Give the location of every parasitized RBC.
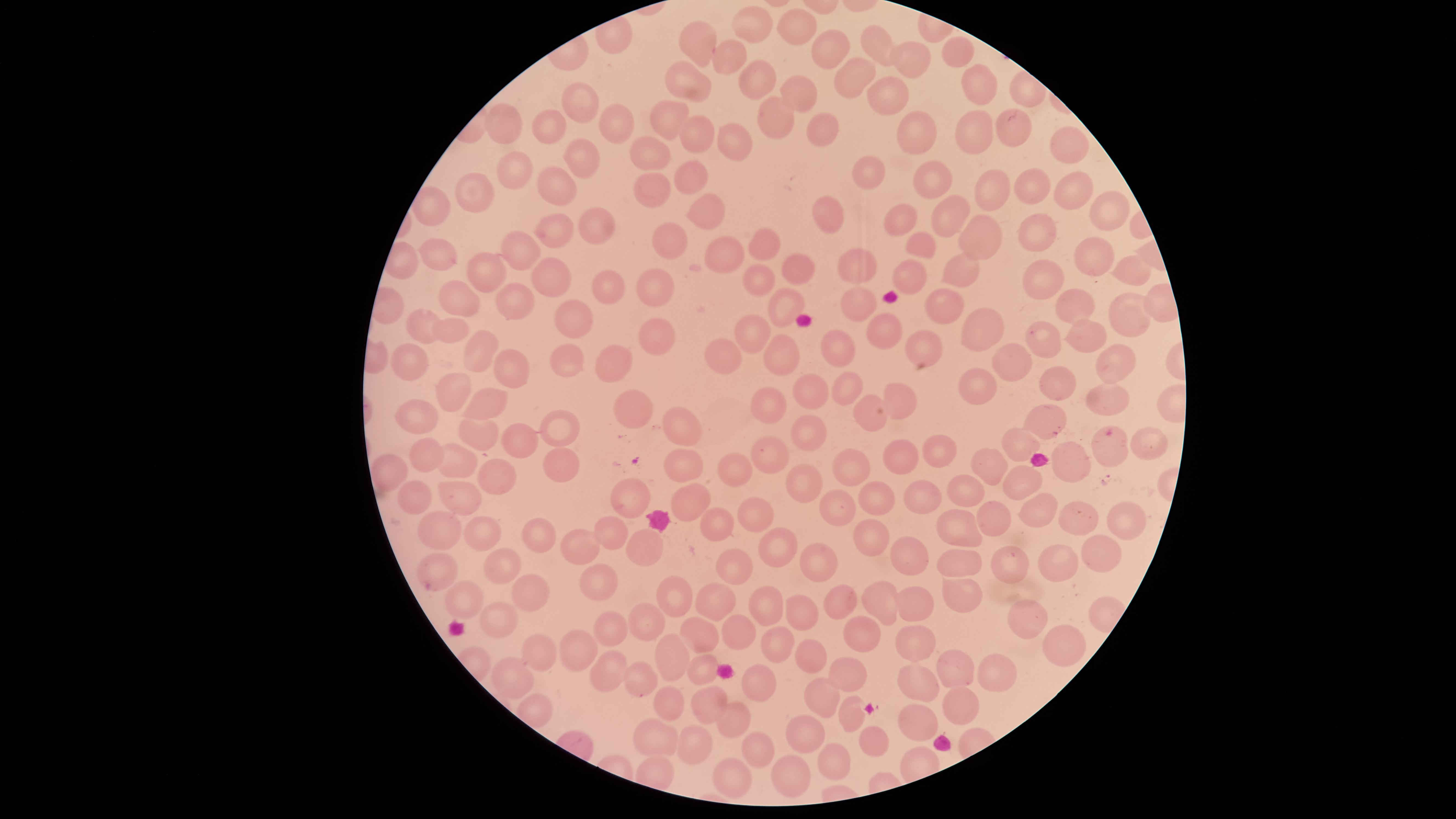
Approximate marker points as (x, y) in pixels.
Parasitized RBCs: (428, 586).

Approximate marker points as (x, y) in pixels. Uninfected RBCs: (754, 24), (801, 28), (699, 37), (875, 45), (831, 47), (960, 49), (729, 55), (913, 57), (851, 75), (755, 81), (688, 83), (976, 86), (799, 88), (883, 95), (578, 110), (666, 116), (774, 119), (615, 126), (817, 126), (1009, 127), (691, 129), (912, 129), (549, 131), (975, 132), (508, 133), (738, 136), (1066, 144), (656, 145), (579, 156), (519, 168), (688, 169), (872, 173), (931, 177), (557, 182), (654, 184), (1033, 187), (478, 190), (989, 190), (1063, 190), (707, 206), (1106, 206), (832, 209), (954, 216), (901, 221), (597, 225), (1039, 227), (557, 232), (980, 235), (667, 237), (923, 247), (730, 248), (765, 248), (441, 253), (518, 255), (1091, 257), (852, 264), (959, 267), (487, 268), (1130, 270), (798, 272), (760, 276), (910, 276), (553, 277), (1041, 277), (602, 284), (660, 285), (464, 296), (511, 302), (784, 304), (862, 304), (1072, 306), (944, 308), (1122, 309), (429, 320), (573, 320), (983, 324), (455, 328), (660, 333), (886, 334), (758, 335), (1048, 338), (1086, 338), (929, 342), (835, 343), (482, 344), (571, 354), (787, 354), (727, 359), (1116, 359), (1012, 361), (412, 362), (617, 364), (510, 370), (1056, 379), (979, 382), (847, 386), (459, 388), (813, 388), (898, 397), (1102, 399), (773, 403), (488, 404), (640, 406), (874, 409), (418, 414), (563, 417), (1046, 422), (685, 423), (806, 429), (481, 431), (525, 436), (1027, 441), (1148, 444), (428, 450), (939, 451), (1107, 452), (768, 457), (1073, 457), (906, 458), (982, 462), (455, 463), (558, 463), (857, 465), (736, 467), (494, 471), (683, 472), (391, 473), (1021, 479), (803, 482), (973, 487), (925, 492), (410, 495), (465, 495), (876, 497), (628, 498), (690, 503), (841, 506), (755, 510), (1037, 511), (1075, 517), (991, 520), (717, 524), (1116, 525), (957, 526), (440, 529), (477, 533), (538, 533), (612, 534), (873, 540), (581, 543), (644, 545), (778, 545), (1093, 546), (909, 550), (967, 556), (813, 562), (1052, 562), (724, 563), (1016, 563), (501, 567), (598, 581), (954, 595), (672, 596), (527, 597), (839, 597), (466, 599), (879, 599), (716, 600), (769, 601), (920, 608), (803, 610), (1030, 615), (494, 624), (650, 627), (611, 628), (703, 628), (743, 635), (865, 635), (775, 636), (915, 645), (813, 647), (1057, 647), (538, 650), (577, 652), (671, 652), (961, 665), (606, 669), (848, 672), (1009, 672), (705, 673), (508, 677), (637, 678), (923, 680), (759, 686), (828, 693), (669, 698), (711, 703), (958, 707), (924, 715), (737, 717), (856, 720), (656, 733), (803, 735), (875, 740), (696, 742), (755, 746), (835, 759), (791, 771), (737, 774). Thin blood film. Species: Plasmodium falciparum. Smartphone photograph through the microscope eyepiece. Circular visible region. Giemsa-stained preparation. One field of view of the specimen. Image is 1456×819 pixels.